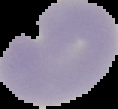
result = no Plasmodium parasites detected
image type = segmented cell region on a black background
preparation = thin blood smear
image size = 118×109 pixels